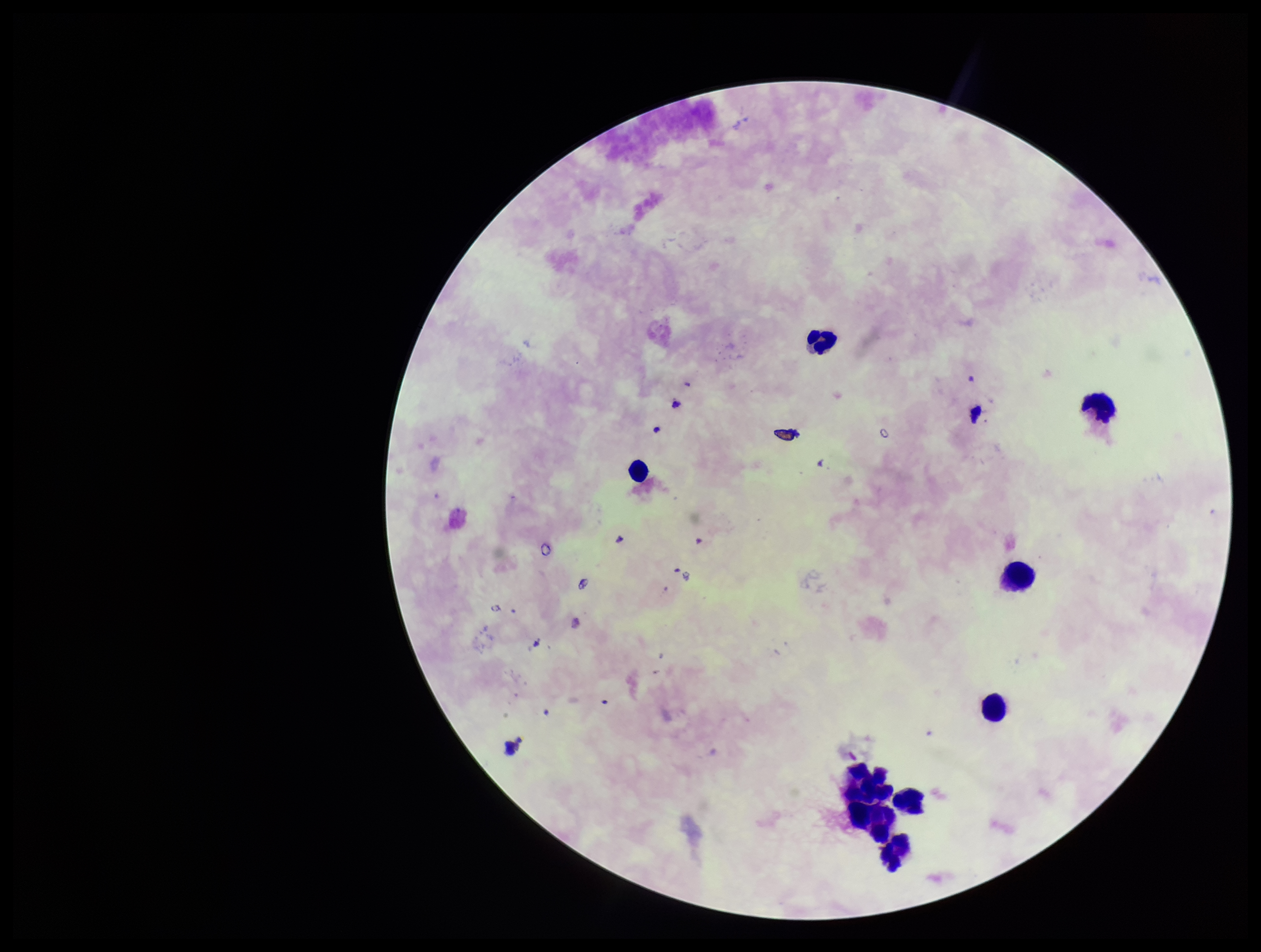

patient malaria status = negative
parasite count = 0
field of view = one from this slide
capture = smartphone photograph through the microscope eyepiece
image size = 1261×952 pixels
leukocyte count = 9
stain = Giemsa
preparation = thick smear
Plasmodium parasites = none detected